Assess this cell for malaria.
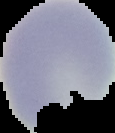

Uninfected.

image size = 115×133 pixels
preparation = thin blood smear
image type = segmented cell region with the area outside set to black